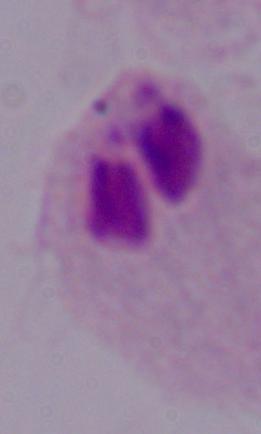

{
  "modality": "micrograph",
  "identification": "trichomonad",
  "magnification": "1000x"
}